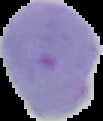
Malaria status: uninfected. Segmented cell region on a black background. Image is 103×121 pixels. From a thin blood film.